Classify this cell by malaria status.
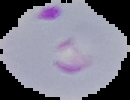

Parasitized.

Summary:
  - Image type: cell region segmented out of the field of view; surrounding area masked to black
  - Image size: 130×100 pixels
  - Preparation: thin blood smear